Assess the morphology of the erythrocytes.
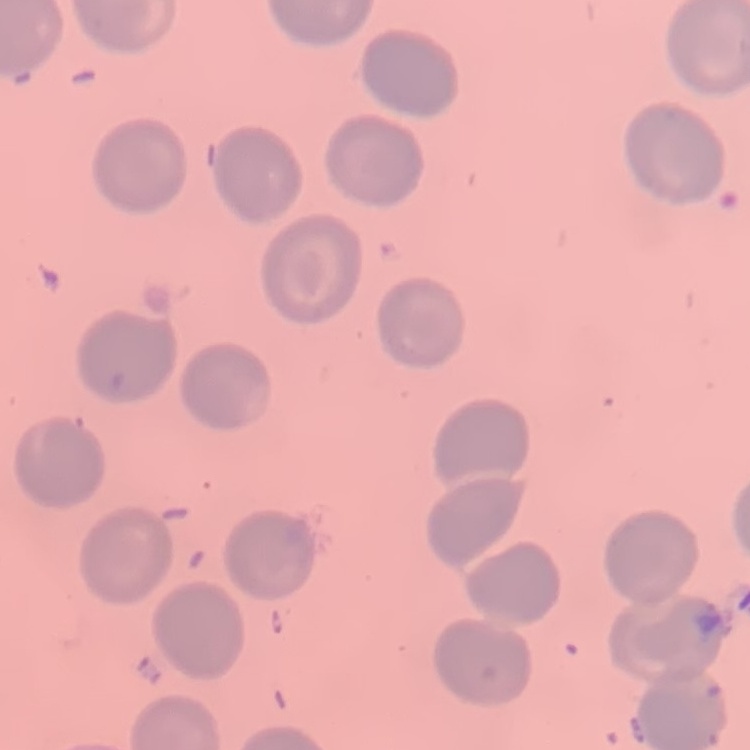
No rouleaux formation.

image type = one tile cut from a larger photomicrograph
preparation = thin peripheral smear
stain = Field's or Giemsa